Comment on the morphology of the red blood cells.
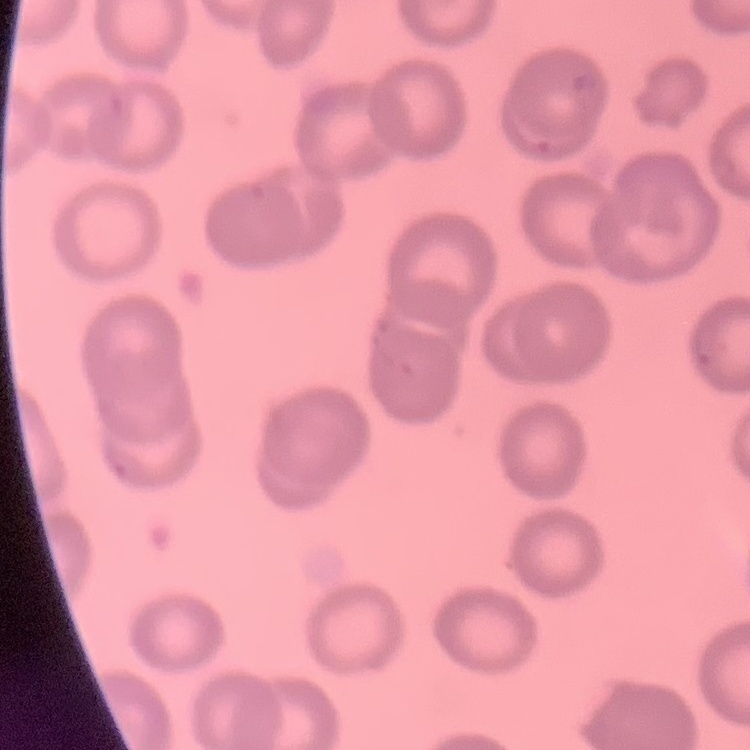

They show no rouleaux formation.

Field's or Giemsa stain. Thin peripheral smear. One tile cut from a larger photomicrograph.